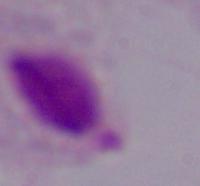
Summary:
  - Identification: trichomonad
  - Modality: micrograph
  - Magnification: 1000x